Classify this cell by malaria status.
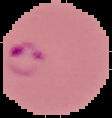

It is parasitized.

preparation: thin blood smear
image_size: 112×118 pixels
image_type: segmented cell region on a black background